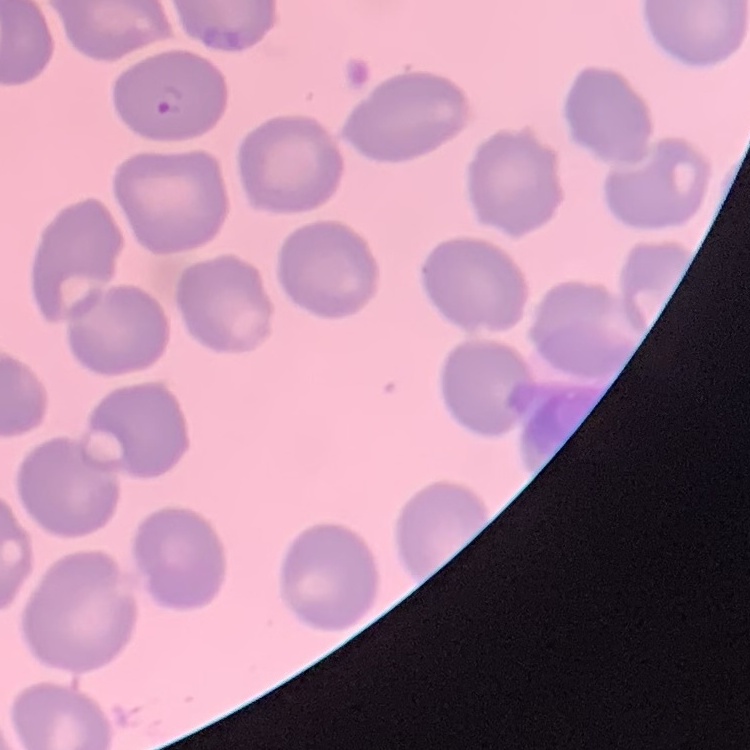
The erythrocytes exhibit no rouleaux formation. Field's or Giemsa stain. One tile cut from a larger photomicrograph. Thin blood film.